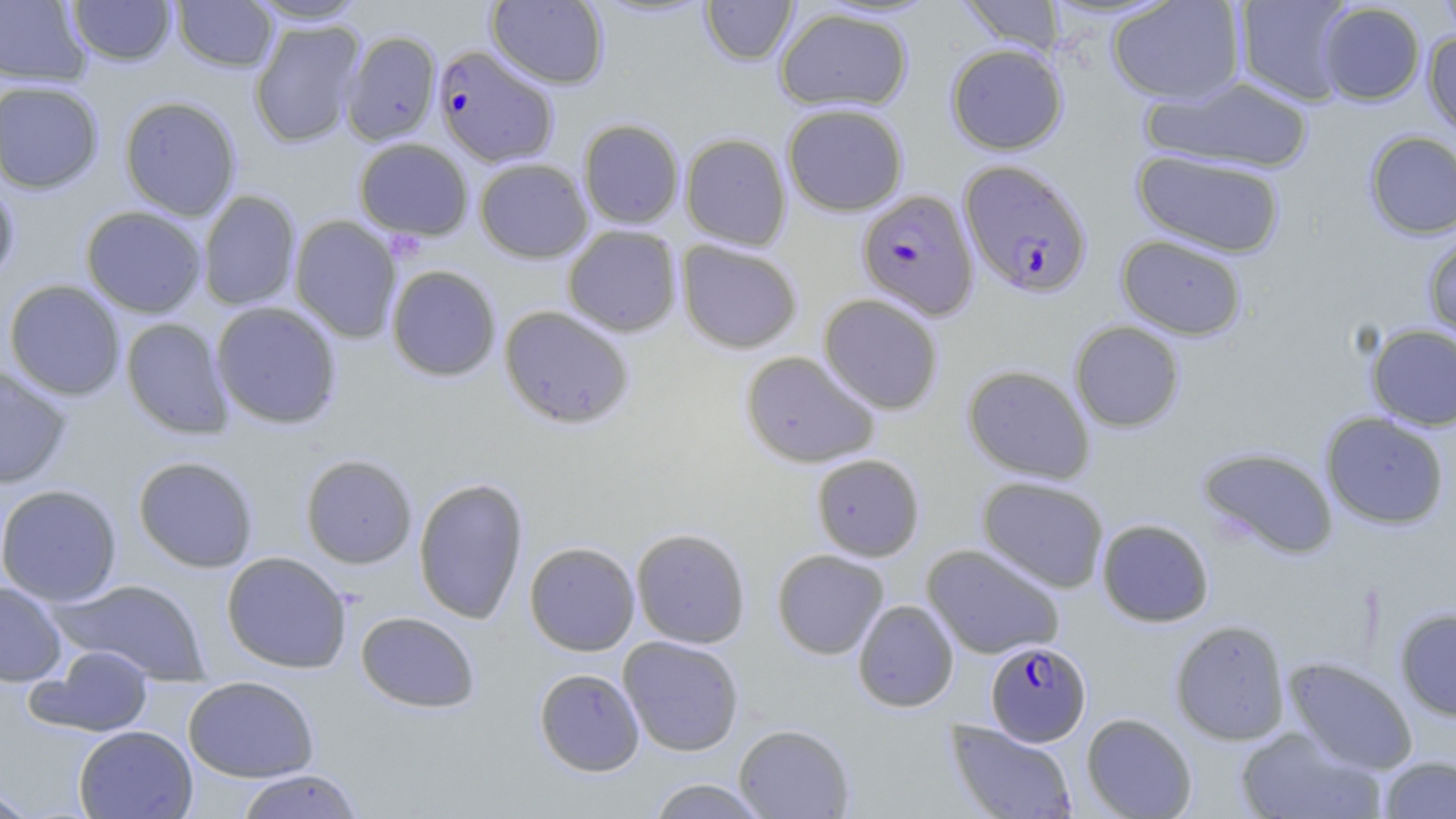
Approximate bounding boxes as named x1/y1/x2/y2 corners in pixels. Plasmodium falciparum-infected red blood cell locations: (x1=433, y1=45, x2=560, y2=167), (x1=959, y1=159, x2=1093, y2=299), (x1=856, y1=189, x2=979, y2=321), (x1=985, y1=640, x2=1091, y2=746). Uninfected red blood cell locations: (x1=0, y1=0, x2=91, y2=86), (x1=67, y1=0, x2=176, y2=66), (x1=172, y1=0, x2=278, y2=72), (x1=244, y1=0, x2=370, y2=24), (x1=486, y1=0, x2=609, y2=89), (x1=955, y1=0, x2=1066, y2=57), (x1=1107, y1=0, x2=1246, y2=104), (x1=1234, y1=0, x2=1358, y2=105), (x1=1435, y1=0, x2=1456, y2=42), (x1=700, y1=1, x2=798, y2=65), (x1=1317, y1=2, x2=1425, y2=105), (x1=774, y1=7, x2=913, y2=112), (x1=249, y1=20, x2=364, y2=148), (x1=342, y1=30, x2=442, y2=146), (x1=1422, y1=30, x2=1456, y2=140), (x1=945, y1=43, x2=1068, y2=155), (x1=1142, y1=75, x2=1315, y2=174), (x1=0, y1=80, x2=104, y2=193), (x1=119, y1=96, x2=241, y2=221), (x1=781, y1=102, x2=908, y2=216), (x1=578, y1=118, x2=685, y2=229), (x1=1364, y1=130, x2=1456, y2=239), (x1=679, y1=132, x2=792, y2=250), (x1=353, y1=138, x2=474, y2=240), (x1=1132, y1=149, x2=1286, y2=258), (x1=474, y1=158, x2=593, y2=263), (x1=0, y1=175, x2=20, y2=287), (x1=197, y1=190, x2=301, y2=311), (x1=81, y1=206, x2=207, y2=317), (x1=289, y1=215, x2=402, y2=343), (x1=562, y1=225, x2=682, y2=337), (x1=1422, y1=232, x2=1456, y2=345), (x1=1115, y1=234, x2=1247, y2=340), (x1=676, y1=240, x2=803, y2=354), (x1=386, y1=264, x2=501, y2=381), (x1=4, y1=279, x2=126, y2=400), (x1=819, y1=293, x2=944, y2=414), (x1=210, y1=301, x2=342, y2=430), (x1=498, y1=305, x2=635, y2=429), (x1=120, y1=317, x2=234, y2=439), (x1=1069, y1=321, x2=1185, y2=433), (x1=1365, y1=323, x2=1456, y2=431), (x1=741, y1=351, x2=880, y2=468), (x1=962, y1=364, x2=1095, y2=484), (x1=0, y1=367, x2=71, y2=488), (x1=1320, y1=411, x2=1449, y2=530), (x1=1197, y1=446, x2=1339, y2=559), (x1=811, y1=453, x2=925, y2=561), (x1=300, y1=454, x2=417, y2=568), (x1=132, y1=455, x2=259, y2=573), (x1=977, y1=475, x2=1109, y2=593), (x1=413, y1=477, x2=529, y2=624), (x1=0, y1=484, x2=122, y2=606), (x1=1096, y1=518, x2=1214, y2=627), (x1=631, y1=527, x2=751, y2=649), (x1=524, y1=541, x2=640, y2=656), (x1=921, y1=544, x2=1066, y2=659), (x1=772, y1=549, x2=889, y2=659), (x1=221, y1=551, x2=352, y2=673), (x1=55, y1=578, x2=211, y2=684), (x1=0, y1=581, x2=67, y2=686), (x1=852, y1=599, x2=959, y2=713), (x1=1394, y1=608, x2=1456, y2=721), (x1=355, y1=611, x2=481, y2=713), (x1=1170, y1=620, x2=1290, y2=745), (x1=618, y1=636, x2=744, y2=756), (x1=32, y1=645, x2=155, y2=737), (x1=1283, y1=657, x2=1418, y2=774), (x1=533, y1=667, x2=645, y2=776), (x1=183, y1=676, x2=319, y2=782), (x1=1081, y1=713, x2=1197, y2=818), (x1=944, y1=719, x2=1079, y2=819), (x1=734, y1=724, x2=855, y2=818), (x1=73, y1=725, x2=198, y2=818), (x1=1235, y1=726, x2=1385, y2=819), (x1=1379, y1=755, x2=1456, y2=818), (x1=234, y1=769, x2=364, y2=819), (x1=646, y1=778, x2=771, y2=818), (x1=0, y1=785, x2=39, y2=818). Slide-level diagnosis: Plasmodium falciparum. May-Grünwald-Giemsa stain. Image is 1456×819 pixels. Thin blood smear. 1000x magnification. One field of a larger specimen. Optical microscopy.